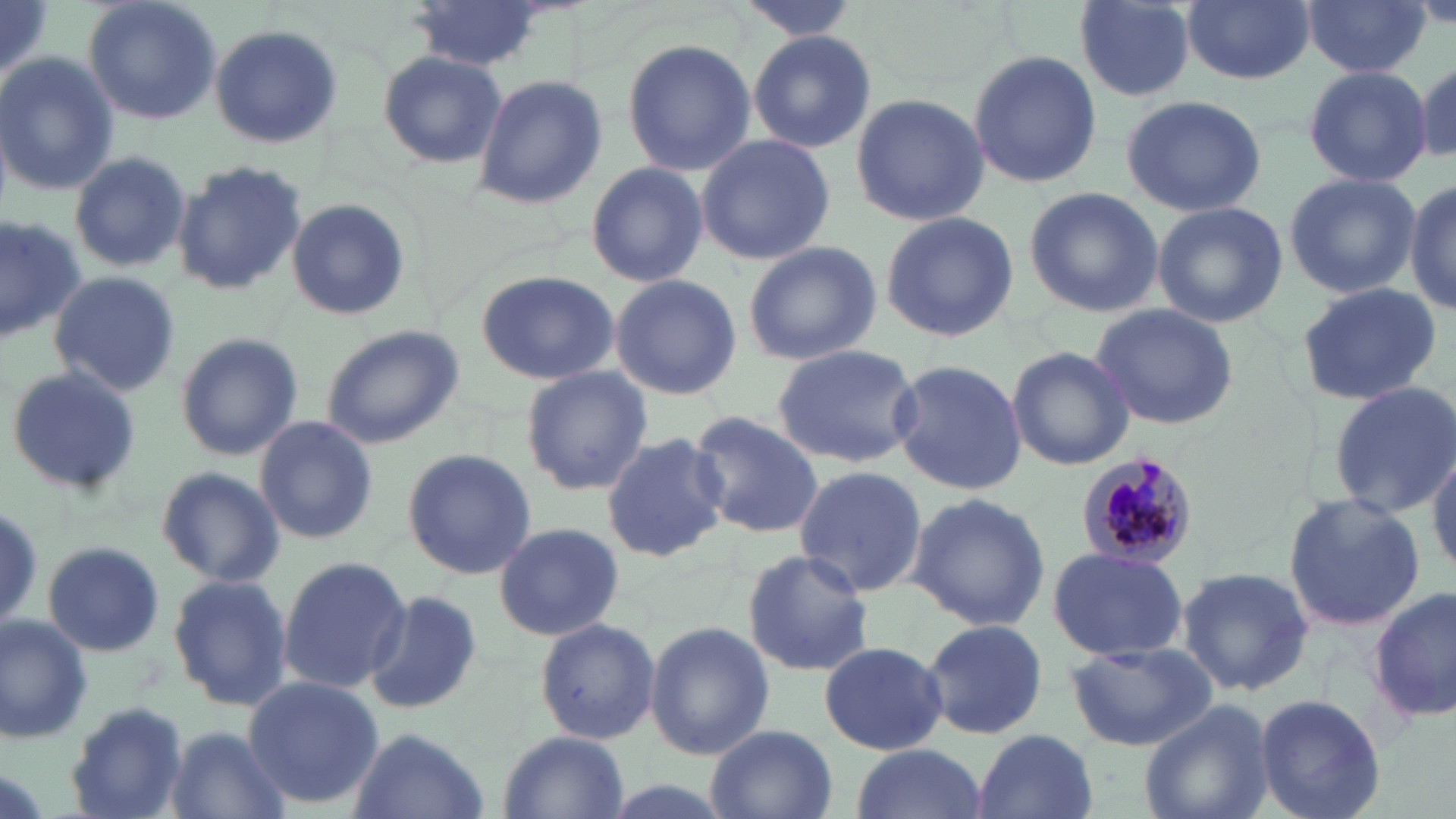
Summary:
  - Coordinate format: approximate bounding boxes as (x1,y1)-(x2,y2) corner pairs in pixels
  - Plasmodium malariae-infected red blood cell locations: (1077,453)-(1199,569)
  - Uninfected red blood cell locations: (80,0)-(223,126), (407,0)-(557,74), (735,0)-(864,39), (1071,0)-(1197,101), (1180,0)-(1315,85), (1,1)-(52,90), (1301,1)-(1431,79), (210,23)-(342,149), (746,29)-(877,154), (623,38)-(758,179), (967,49)-(1100,188), (376,50)-(506,169), (0,54)-(119,196), (1412,54)-(1455,167), (1302,65)-(1431,186), (472,74)-(608,211), (848,92)-(989,228), (1120,94)-(1267,217), (695,134)-(836,266), (68,150)-(191,275), (173,158)-(305,294), (585,162)-(708,286), (1282,172)-(1420,299), (1407,173)-(1456,317), (1023,186)-(1164,318), (286,198)-(410,322), (1151,201)-(1286,326), (0,210)-(87,344), (878,210)-(1019,343), (742,240)-(881,366), (46,270)-(182,396), (476,270)-(620,385), (611,275)-(741,399), (1294,280)-(1446,405), (1089,302)-(1241,431), (319,322)-(465,449), (175,332)-(303,462), (770,343)-(923,465), (1005,347)-(1135,470), (889,358)-(1027,497), (6,365)-(145,499), (519,366)-(654,496), (1328,380)-(1456,519), (687,409)-(822,541), (254,416)-(378,546), (603,429)-(729,564), (1429,445)-(1456,576), (401,448)-(538,581), (793,463)-(927,598), (154,464)-(287,587), (906,490)-(1051,630), (1282,491)-(1426,632), (494,522)-(625,642), (40,541)-(165,658), (1046,545)-(1190,661), (740,548)-(875,677), (276,556)-(411,692), (1176,564)-(1315,695), (165,572)-(294,712), (1373,585)-(1456,723), (363,588)-(484,717), (0,611)-(96,745), (533,615)-(661,746), (921,618)-(1049,742), (644,620)-(773,761), (817,639)-(948,755), (1065,641)-(1216,751), (243,673)-(383,810), (1256,694)-(1387,819), (1136,699)-(1276,819), (67,702)-(190,819), (704,724)-(837,819), (165,727)-(289,819), (348,727)-(489,819), (972,729)-(1097,819), (496,731)-(630,818), (849,744)-(988,819)
  - Slide-level diagnosis: Plasmodium malariae
  - Preparation: thin blood smear
  - Magnification: 1000x
  - Modality: optical microscopy
  - Field of view: one of a larger specimen
  - Image size: 1456×819 pixels
  - Stain: May-Grünwald-Giemsa